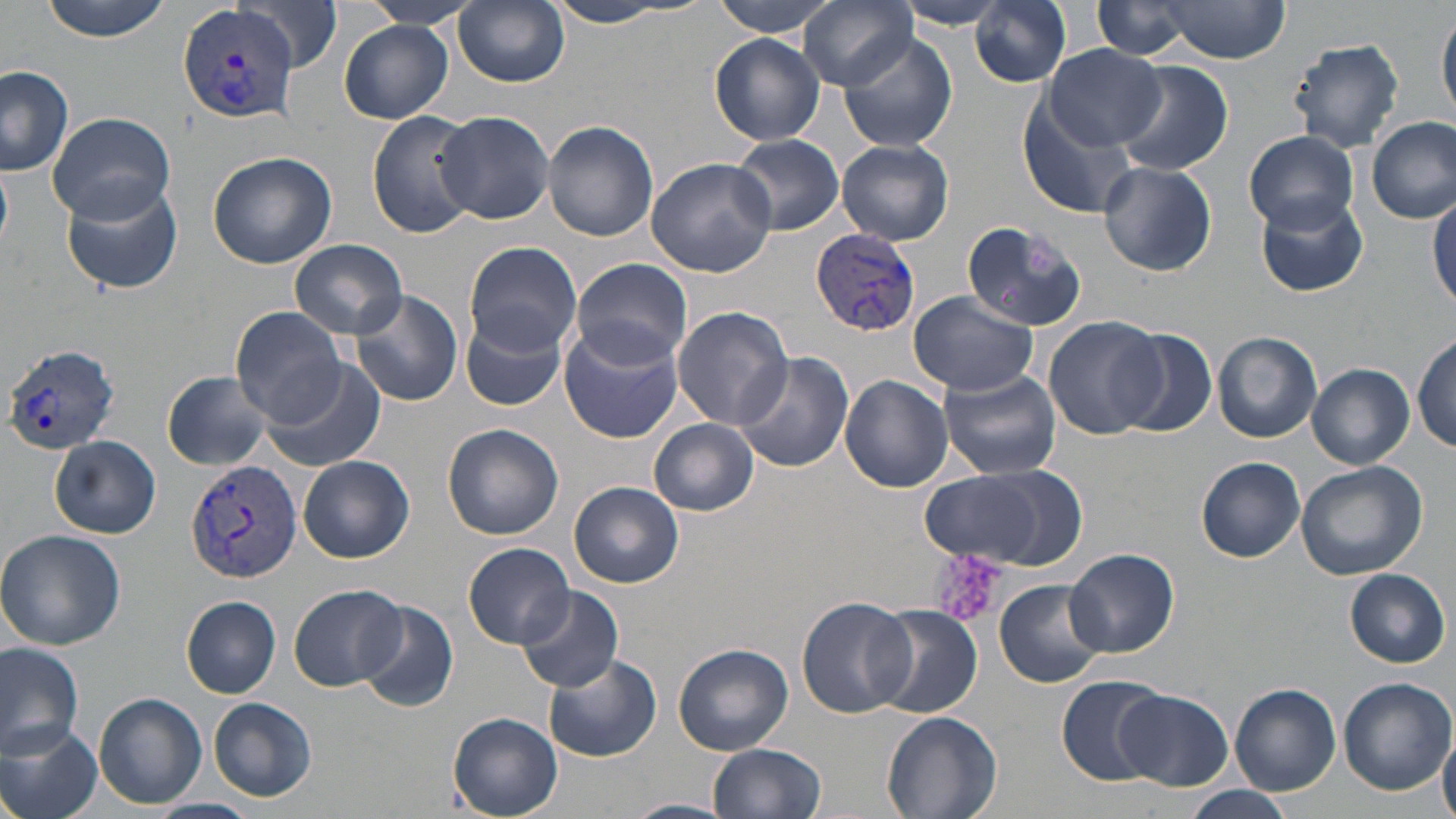

Summary:
  - Coordinate format: approximate bounding boxes as named x1/y1/x2/y2 corners in pixels
  - Plasmodium vivax-infected red blood cell locations: (x1=178, y1=3, x2=301, y2=125), (x1=812, y1=229, x2=921, y2=338), (x1=4, y1=343, x2=122, y2=456), (x1=186, y1=458, x2=301, y2=582)
  - Uninfected red blood cell locations: (x1=37, y1=0, x2=174, y2=41), (x1=239, y1=0, x2=342, y2=72), (x1=455, y1=0, x2=569, y2=87), (x1=714, y1=0, x2=841, y2=36), (x1=800, y1=0, x2=917, y2=90), (x1=970, y1=0, x2=1072, y2=86), (x1=360, y1=1, x2=478, y2=31), (x1=1091, y1=1, x2=1200, y2=59), (x1=1158, y1=2, x2=1288, y2=62), (x1=540, y1=3, x2=686, y2=28), (x1=894, y1=3, x2=1015, y2=29), (x1=1438, y1=12, x2=1456, y2=121), (x1=340, y1=20, x2=452, y2=123), (x1=838, y1=31, x2=958, y2=152), (x1=709, y1=34, x2=826, y2=146), (x1=1288, y1=39, x2=1405, y2=151), (x1=1042, y1=44, x2=1166, y2=148), (x1=1114, y1=62, x2=1233, y2=180), (x1=0, y1=66, x2=76, y2=177), (x1=1017, y1=98, x2=1141, y2=221), (x1=434, y1=110, x2=554, y2=225), (x1=46, y1=111, x2=177, y2=223), (x1=367, y1=111, x2=481, y2=238), (x1=1367, y1=115, x2=1455, y2=224), (x1=542, y1=120, x2=660, y2=243), (x1=1245, y1=130, x2=1359, y2=232), (x1=731, y1=134, x2=844, y2=235), (x1=838, y1=140, x2=954, y2=245), (x1=207, y1=151, x2=336, y2=268), (x1=646, y1=157, x2=777, y2=277), (x1=1099, y1=160, x2=1216, y2=276), (x1=0, y1=163, x2=13, y2=251), (x1=60, y1=177, x2=182, y2=294), (x1=1429, y1=189, x2=1456, y2=310), (x1=1256, y1=193, x2=1368, y2=297), (x1=960, y1=219, x2=1090, y2=332), (x1=919, y1=238, x2=1061, y2=373), (x1=290, y1=239, x2=407, y2=339), (x1=463, y1=241, x2=581, y2=356), (x1=569, y1=257, x2=693, y2=371), (x1=351, y1=289, x2=463, y2=406), (x1=909, y1=292, x2=1038, y2=394), (x1=230, y1=306, x2=345, y2=425), (x1=672, y1=306, x2=793, y2=429), (x1=460, y1=312, x2=569, y2=411), (x1=1044, y1=315, x2=1166, y2=440), (x1=560, y1=328, x2=683, y2=444), (x1=1113, y1=328, x2=1219, y2=439), (x1=1213, y1=330, x2=1322, y2=442), (x1=1412, y1=334, x2=1455, y2=451), (x1=732, y1=350, x2=854, y2=473), (x1=259, y1=361, x2=386, y2=472), (x1=1308, y1=363, x2=1413, y2=468), (x1=938, y1=368, x2=1062, y2=480), (x1=161, y1=370, x2=276, y2=470), (x1=840, y1=374, x2=954, y2=493), (x1=649, y1=419, x2=759, y2=515), (x1=442, y1=423, x2=564, y2=540), (x1=51, y1=437, x2=161, y2=538), (x1=299, y1=455, x2=413, y2=563), (x1=1197, y1=457, x2=1306, y2=562), (x1=1295, y1=461, x2=1427, y2=580), (x1=918, y1=467, x2=1080, y2=570), (x1=570, y1=481, x2=684, y2=587), (x1=0, y1=529, x2=127, y2=649), (x1=464, y1=543, x2=575, y2=650), (x1=1066, y1=548, x2=1179, y2=657), (x1=1345, y1=568, x2=1451, y2=668), (x1=995, y1=579, x2=1104, y2=689), (x1=516, y1=584, x2=624, y2=692), (x1=289, y1=585, x2=410, y2=692), (x1=182, y1=596, x2=280, y2=698), (x1=797, y1=596, x2=916, y2=719), (x1=356, y1=600, x2=460, y2=714), (x1=870, y1=607, x2=984, y2=718), (x1=0, y1=640, x2=84, y2=754), (x1=672, y1=644, x2=793, y2=755), (x1=545, y1=652, x2=661, y2=763), (x1=1056, y1=675, x2=1169, y2=785), (x1=1338, y1=678, x2=1454, y2=795), (x1=1230, y1=684, x2=1340, y2=794), (x1=1114, y1=691, x2=1233, y2=791), (x1=94, y1=692, x2=205, y2=809), (x1=209, y1=697, x2=315, y2=800), (x1=882, y1=711, x2=1003, y2=819), (x1=447, y1=713, x2=564, y2=819), (x1=1, y1=723, x2=103, y2=819), (x1=1438, y1=726, x2=1456, y2=819), (x1=706, y1=742, x2=827, y2=819), (x1=1175, y1=785, x2=1298, y2=819), (x1=146, y1=797, x2=259, y2=819), (x1=623, y1=798, x2=737, y2=819)
  - Platelet locations: (x1=930, y1=549, x2=1006, y2=627)
  - Slide-level diagnosis: Plasmodium vivax
  - Field of view: single
  - Modality: light microscopy
  - Magnification: 1000x
  - Preparation: thin blood film
  - Image size: 1456×819 pixels
  - Stain: May-Grünwald-Giemsa